Outline each blood parasite and name the species.
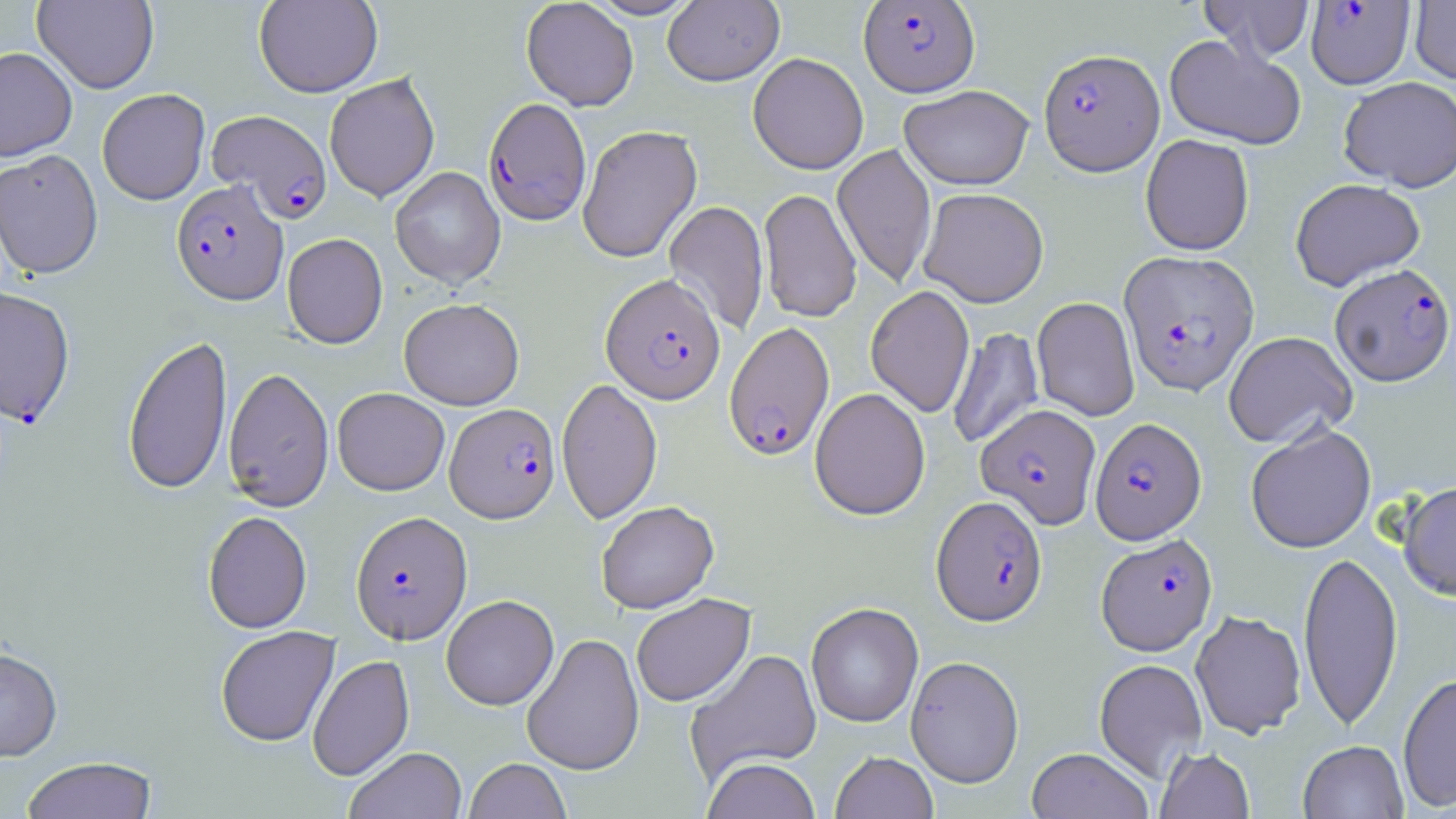

Approximate bounding boxes as [x1, y1, x2, y2] in pixels.
Plasmodium falciparum-infected red blood cells (subset): [859, 1, 979, 96], [1306, 1, 1415, 89], [1039, 48, 1165, 175], [483, 98, 592, 226], [205, 109, 332, 221], [171, 180, 288, 306], [1119, 250, 1259, 395], [1330, 263, 1454, 386], [601, 274, 725, 404], [724, 321, 835, 461], [445, 403, 560, 523], [976, 403, 1101, 528], [1090, 417, 1206, 543], [932, 495, 1047, 626], [350, 511, 473, 644], [1096, 533, 1218, 655].
No Plasmodium ovale, Plasmodium malariae, Plasmodium vivax, Babesia divergens, or Trypanosoma brucei observed.

Uninfected red blood cell locations (subset): [254, 0, 383, 97], [521, 0, 639, 111], [586, 0, 702, 20], [662, 0, 784, 86], [1199, 0, 1314, 60], [32, 1, 159, 94], [1410, 1, 1456, 84], [1164, 34, 1306, 150], [0, 47, 78, 161], [748, 52, 868, 174], [324, 73, 439, 202], [1339, 76, 1456, 192], [898, 84, 1033, 190], [97, 88, 210, 205], [578, 125, 702, 263], [1140, 134, 1254, 255], [832, 144, 936, 289], [0, 149, 104, 279], [390, 167, 506, 289], [1290, 178, 1426, 291], [919, 187, 1049, 307], [759, 188, 862, 323], [663, 200, 769, 335], [282, 233, 388, 349], [865, 286, 975, 418], [1031, 296, 1140, 422], [399, 298, 524, 410], [947, 327, 1044, 449], [1223, 331, 1358, 449], [122, 334, 233, 495], [223, 367, 334, 512], [556, 377, 662, 524], [333, 387, 449, 495], [810, 387, 930, 520], [1245, 423, 1376, 553], [1398, 479, 1456, 601], [596, 500, 719, 614], [203, 511, 313, 634], [1298, 549, 1403, 731], [631, 593, 755, 707], [441, 594, 559, 710], [806, 602, 923, 727], [1190, 610, 1306, 739], [215, 625, 340, 746], [522, 633, 644, 775], [0, 646, 63, 761], [685, 648, 823, 784], [307, 654, 414, 781], [905, 655, 1024, 787], [1094, 658, 1208, 783], [1398, 672, 1456, 811], [1298, 740, 1408, 818], [345, 746, 467, 819], [1026, 747, 1153, 819], [1155, 747, 1255, 819], [830, 751, 938, 819], [21, 756, 158, 819], [701, 757, 821, 819], [464, 758, 571, 818]. Slide-level diagnosis: Plasmodium falciparum. Captured at 1000x magnification. Light microscopy. Thin blood film. May-Grünwald-Giemsa-stained preparation. One field of a larger specimen. Image is 1456×819 pixels.